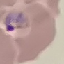
Result: malaria parasites identified. Giemsa-stained preparation. Cell patch, automatically extracted from a larger field of view and resized to 64 × 64 pixels. Thin blood smear. Photographed with a smartphone camera at the microscope eyepiece.